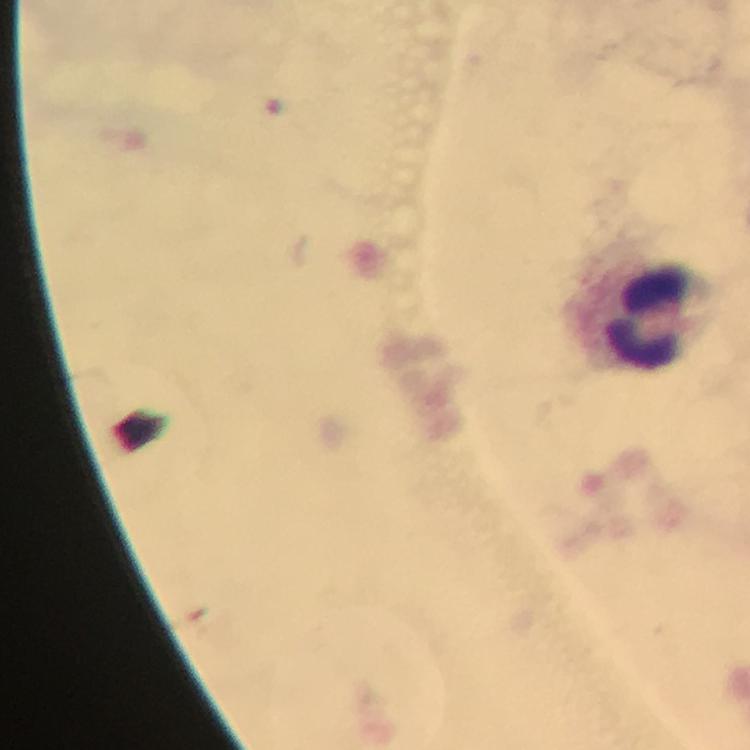 Approximate centers as [x, y] in pixels. Leukocyte locations: [638, 315]. Image is 750×750 pixels. From a diagnostic examination for malaria. 100x magnification. Plasmodium parasites: none seen. Giemsa stain. Immersion oil was used. A crop from one field of view. Thick blood smear. Smartphone photograph taken through a microscope.